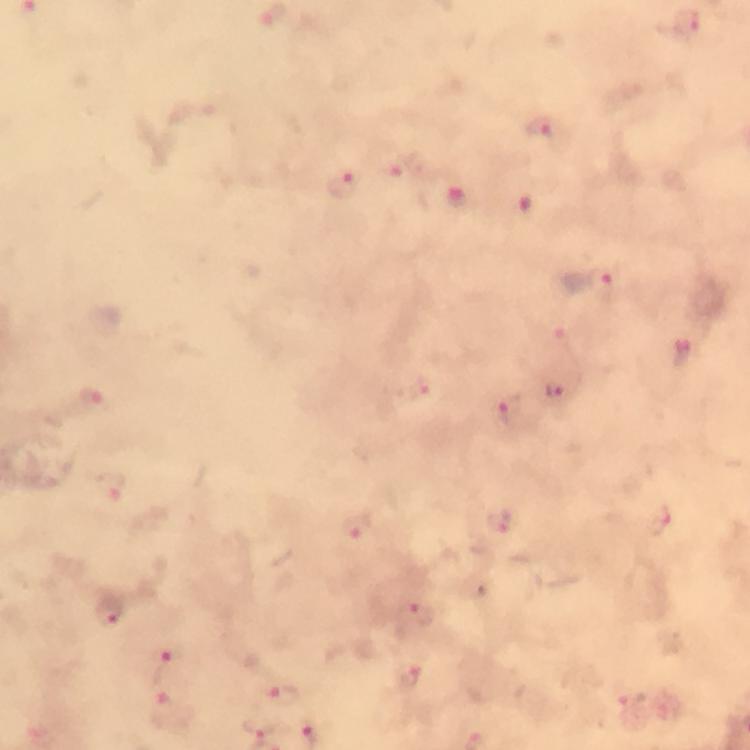 Approximate centers as (x, y) in pixels. Plasmodium parasite locations: (686, 27), (541, 130), (395, 168), (344, 182), (458, 198), (604, 279), (558, 335), (419, 389), (555, 389), (92, 400), (508, 409), (110, 491), (661, 518), (495, 522), (353, 528), (109, 610), (418, 613), (160, 663), (409, 674), (277, 691), (631, 695), (165, 710), (258, 726). Thick smear. Giemsa stain. At 100x magnification. Cropped region of a single field of view. From a diagnostic examination for malaria. Image is 750×750 pixels. Photographed through the microscope with a smartphone camera. Immersion oil was used.